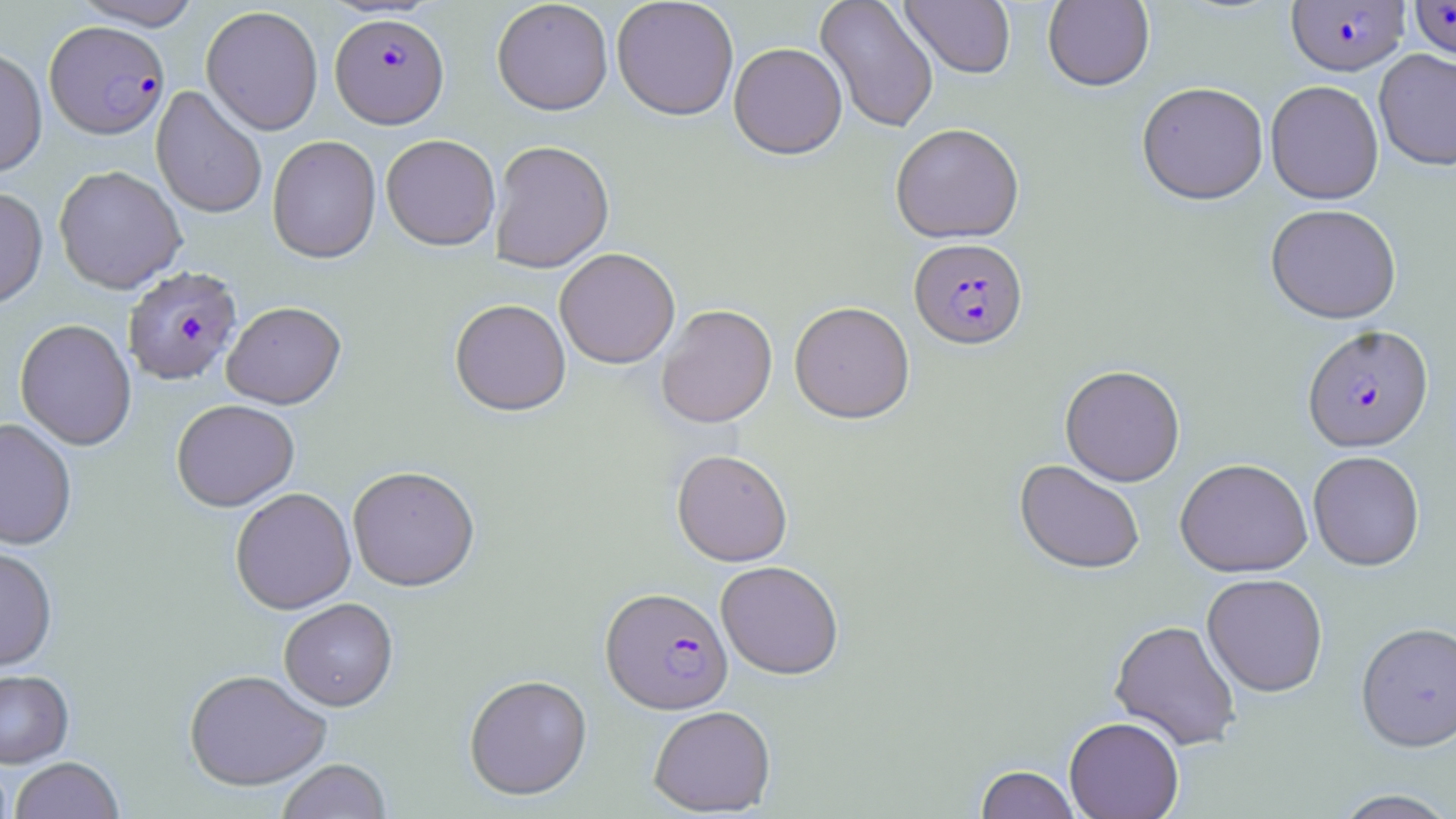

slide_level_diagnosis: Plasmodium falciparum
modality: optical microscopy
image_size: 1456×819 pixels
preparation: thin blood film
magnification: 1000x
uninfected_red_blood_cell_locations: 'approximate bounding boxes as (x1, y1, x2, y2) in pixels: (73, 0, 204, 31), (814, 0, 939, 134), (1042, 0, 1155, 93), (491, 1, 613, 118), (611, 1, 739, 123), (900, 1, 1016, 80), (201, 6, 324, 136), (729, 44, 847, 162), (0, 46, 48, 178), (1373, 49, 1456, 172), (1265, 81, 1384, 205), (1137, 82, 1269, 207), (151, 86, 267, 220), (890, 125, 1025, 245), (266, 136, 381, 266), (381, 136, 500, 253), (489, 142, 615, 275), (53, 166, 187, 295), (0, 187, 48, 311), (1265, 204, 1402, 324), (554, 250, 680, 371), (449, 300, 571, 418), (222, 302, 346, 411), (789, 303, 915, 425), (657, 305, 778, 429), (14, 320, 137, 452), (1060, 366, 1185, 487), (171, 401, 299, 514), (0, 420, 77, 552), (671, 450, 793, 567), (1308, 451, 1425, 571), (1174, 459, 1313, 578), (1014, 460, 1145, 576), (347, 468, 480, 594), (231, 488, 356, 616), (0, 547, 58, 672), (716, 561, 844, 680), (1202, 573, 1328, 698), (279, 600, 398, 712), (1109, 620, 1241, 751), (1356, 622, 1456, 752), (0, 670, 74, 768), (184, 671, 331, 793), (464, 675, 593, 802), (648, 706, 776, 817), (1064, 717, 1184, 819), (9, 758, 123, 819), (277, 760, 392, 819), (0, 762, 12, 819), (975, 765, 1081, 819), (1331, 789, 1456, 818)'
plasmodium_falciparum_infected_red_blood_cell_locations: 'approximate bounding boxes as (x1, y1, x2, y2) in pixels: (1409, 0, 1456, 62), (1285, 1, 1410, 77), (330, 14, 450, 130), (45, 21, 169, 140), (909, 239, 1028, 352), (124, 266, 243, 386), (1302, 324, 1434, 453), (600, 588, 733, 715)'
stain: May-Grünwald-Giemsa
field_of_view: one of a larger specimen